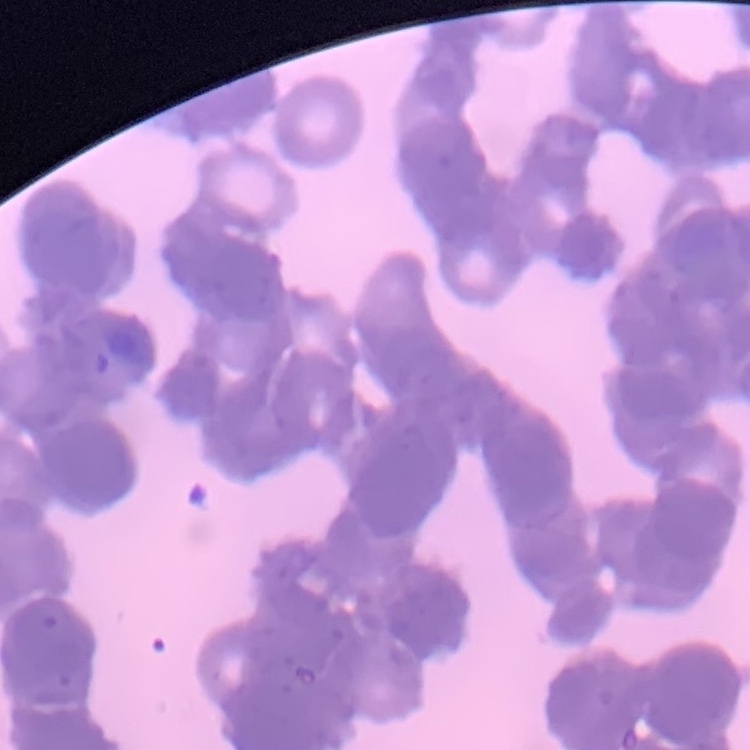

erythrocyte morphology = rouleaux formation
preparation = thin blood smear
image type = square crop of a larger photomicrograph
stain = Field's or Giemsa